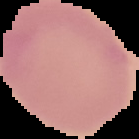
result = no Plasmodium parasites detected
preparation = thin blood smear
image type = cell region segmented out of the field of view; surrounding area masked to black
image size = 139×139 pixels